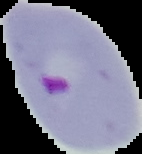

Summary:
  - Malaria status: parasitized
  - Image type: segmented cell region on a black background
  - Image size: 142×154 pixels
  - Preparation: thin blood film